Outline each blood parasite and name the species.
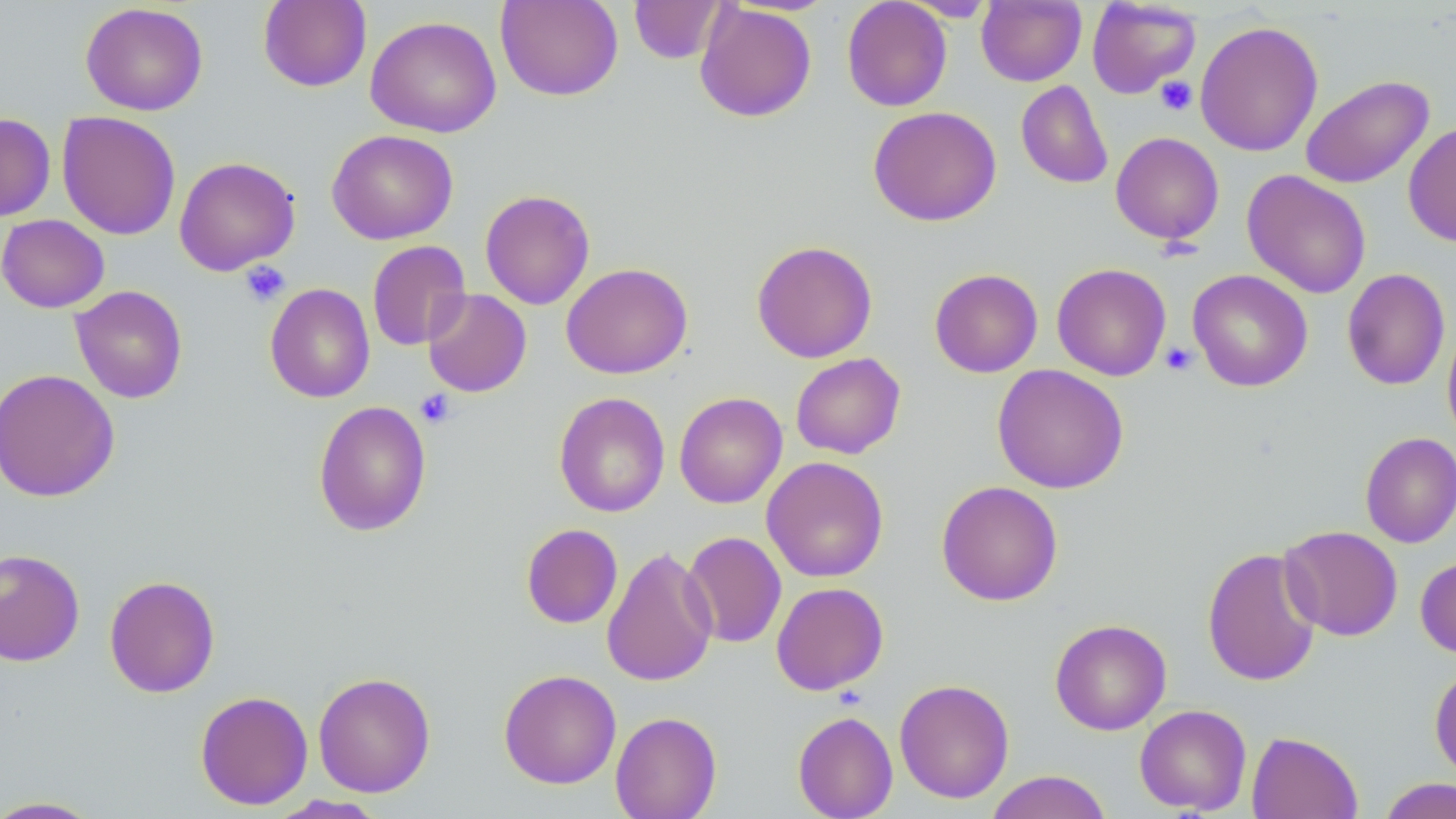

No blood parasites observed.

Summary:
  - Coordinate format: approximate bounding boxes as (x1,y1)-(x2,y2) corner pairs in pixels
  - Uninfected red blood cell locations: (258,0)-(372,92), (495,0)-(623,101), (629,0)-(727,64), (841,0)-(953,112), (898,0)-(999,22), (977,0)-(1086,86), (1087,0)-(1201,98), (80,2)-(208,116), (695,3)-(817,122), (365,15)-(502,138), (1195,20)-(1324,157), (1300,74)-(1434,190), (1016,80)-(1113,189), (868,106)-(1002,227), (57,111)-(181,240), (0,113)-(56,222), (1403,122)-(1456,247), (326,129)-(458,244), (1110,131)-(1225,245), (174,156)-(300,276), (1242,169)-(1372,299), (479,189)-(595,310), (0,214)-(109,312), (367,240)-(471,351), (751,240)-(878,363), (561,262)-(693,379), (1052,263)-(1171,381), (929,268)-(1043,378), (1342,268)-(1450,390), (1187,269)-(1313,392), (264,283)-(375,403), (70,285)-(188,404), (422,288)-(532,398), (1442,322)-(1456,448), (790,352)-(906,459), (992,364)-(1129,494), (0,368)-(120,502), (553,392)-(670,518), (674,392)-(787,508), (313,400)-(432,537), (1360,431)-(1456,548), (762,456)-(889,582), (936,480)-(1063,606), (521,523)-(623,629), (1279,525)-(1403,641), (682,531)-(787,648), (602,545)-(718,688), (1201,546)-(1323,687), (0,548)-(85,667), (1416,554)-(1456,659), (104,575)-(220,698), (771,582)-(889,695), (1049,618)-(1172,735), (1429,663)-(1456,782), (498,668)-(622,789), (313,671)-(436,798), (894,678)-(1015,804), (195,690)-(313,810), (1134,704)-(1252,815), (610,711)-(722,819), (793,711)-(898,819), (1246,731)-(1363,819), (985,770)-(1113,819), (1377,777)-(1456,818), (268,795)-(388,818), (0,796)-(104,818)
  - Platelet locations: (1156,76)-(1197,116), (239,260)-(290,307), (1161,342)-(1197,375), (416,389)-(456,428)
  - Slide-level diagnosis: no evidence of blood parasites
  - Stain: May-Grünwald-Giemsa
  - Magnification: 1000x
  - Field of view: one of a larger specimen
  - Modality: optical microscopy
  - Image size: 1456×819 pixels
  - Preparation: thin blood film